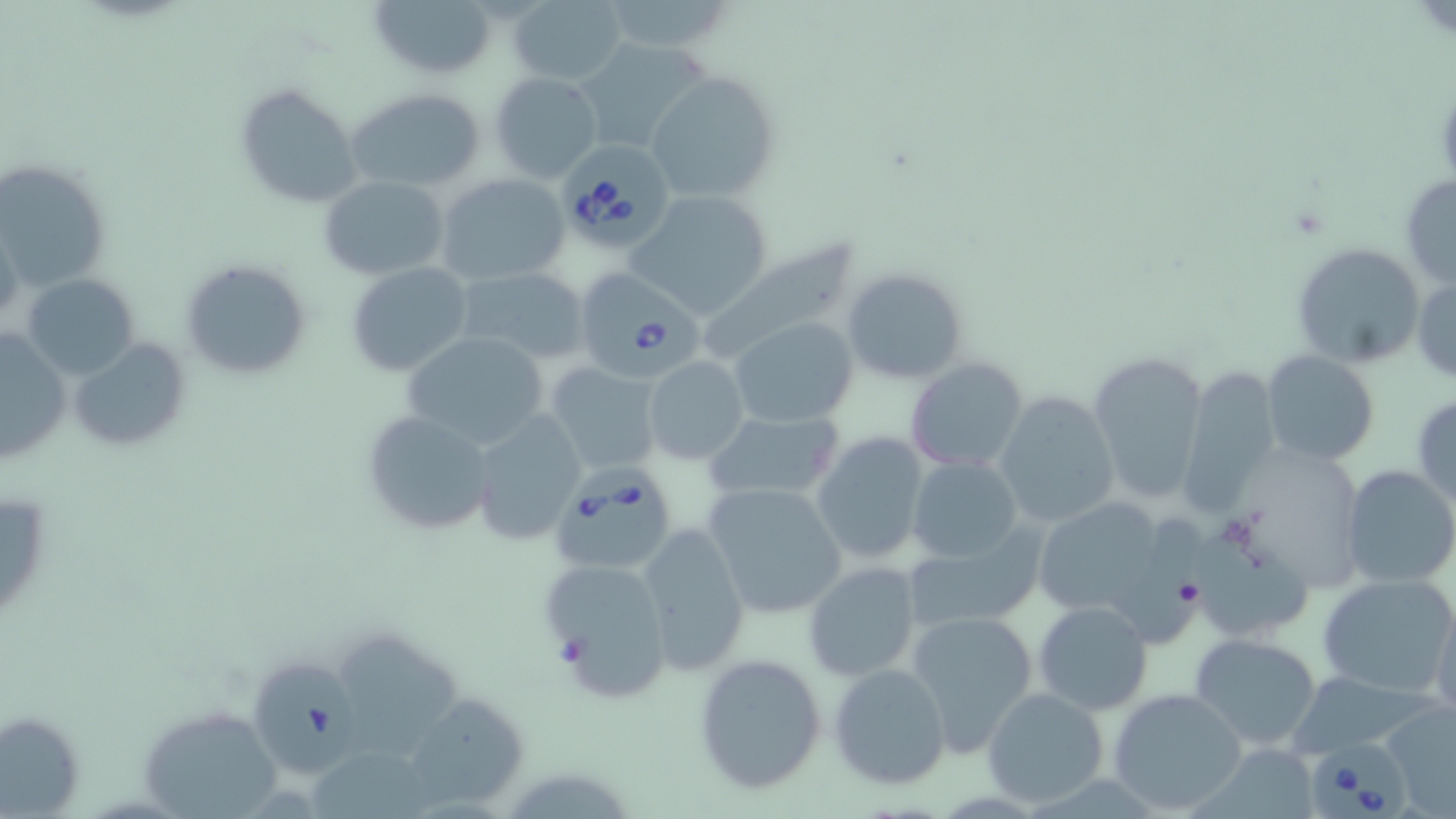

{
  "slide_level_diagnosis": "Babesia divergens",
  "modality": "light microscopy",
  "image_size": "1456×819 pixels",
  "preparation": "thin blood smear",
  "field_of_view": "one of a larger specimen",
  "stain": "May-Grünwald-Giemsa",
  "uninfected_red_blood_cell_locations": "approximate bounding boxes as [x1, y1, x2, y2] in pixels: [368, 0, 495, 80], [597, 0, 737, 56], [509, 1, 627, 85], [575, 37, 712, 156], [645, 68, 779, 202], [490, 73, 604, 184], [235, 82, 363, 207], [346, 89, 487, 192], [0, 158, 111, 290], [435, 173, 571, 287], [319, 175, 449, 278], [1400, 175, 1456, 291], [628, 192, 775, 316], [690, 236, 866, 362], [1291, 241, 1426, 369], [178, 257, 309, 382], [347, 262, 473, 377], [456, 267, 590, 364], [840, 268, 968, 385], [1412, 272, 1456, 383], [24, 273, 140, 375], [730, 318, 858, 426], [1, 326, 71, 464], [403, 331, 549, 448], [69, 337, 190, 451], [1085, 349, 1211, 507], [1261, 350, 1380, 465], [643, 357, 749, 465], [906, 358, 1029, 472], [544, 362, 664, 477], [1177, 365, 1283, 514], [994, 390, 1121, 528], [1412, 395, 1456, 511], [359, 409, 494, 536], [702, 409, 846, 504], [472, 411, 588, 544], [811, 432, 930, 566], [909, 456, 1023, 563], [1340, 466, 1456, 589], [701, 483, 848, 619], [0, 486, 54, 630], [1027, 494, 1179, 629], [1115, 508, 1204, 651], [1193, 522, 1311, 635], [634, 524, 751, 673], [900, 525, 1043, 637], [538, 557, 674, 704], [802, 560, 922, 682], [1318, 573, 1456, 697], [1034, 601, 1152, 716], [1430, 603, 1456, 720], [905, 608, 1038, 754], [346, 631, 481, 773], [1191, 633, 1325, 751], [691, 651, 828, 795], [827, 662, 951, 789], [1292, 677, 1436, 756], [982, 686, 1108, 806], [1108, 688, 1248, 814], [401, 691, 528, 812], [1382, 701, 1455, 810], [133, 706, 284, 816], [0, 710, 85, 815], [1197, 742, 1318, 818], [306, 743, 429, 819]",
  "babesia_divergens_infected_red_blood_cell_locations": "approximate bounding boxes as [x1, y1, x2, y2] in pixels: [559, 151, 670, 246], [576, 268, 715, 379], [549, 472, 679, 574], [252, 658, 357, 780], [1308, 733, 1415, 819]",
  "magnification": "1000x"
}